Locate every Plasmodium falciparum parasite and give its life-cycle stage, and locate every leukocyte and any debris.
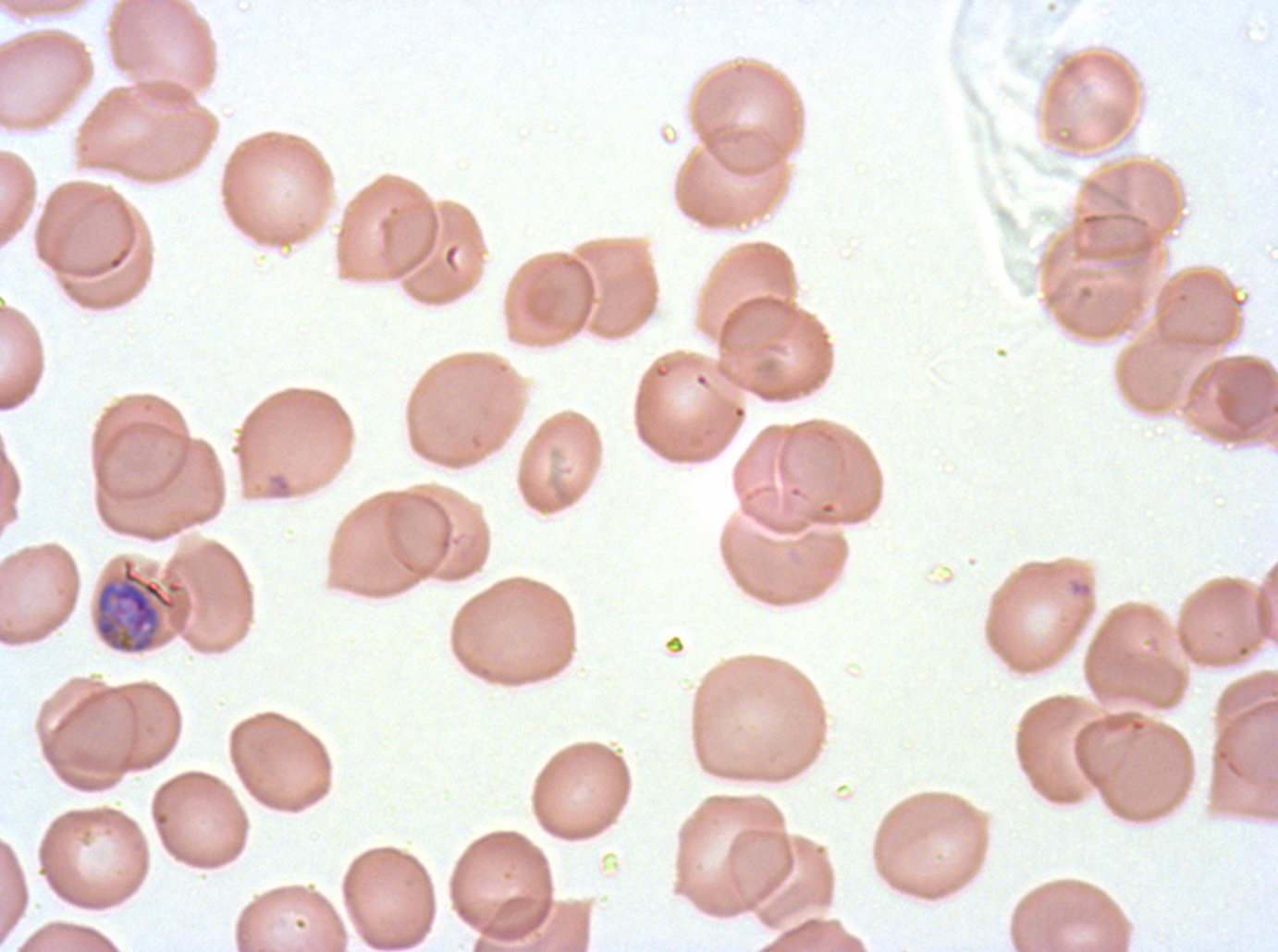
Approximate bounding boxes as {x1, y1, x2, y2} in pixels.
Late trophozoites: {93, 557, 178, 654}.
No rings, late-ring/early-trophozoite forms, mid trophozoites, early schizonts, late schizonts, segmenters, gametocytes, leukocytes, or debris observed.

Summary:
  - Stain: Giemsa
  - Specimen: Plasmodium falciparum cultured ex vivo for 24 to 48 hours, from a patient in The Gambia
  - Preparation: thin blood smear
  - Field of view: one sub-image of a larger composite
  - Image size: 1278×952 pixels